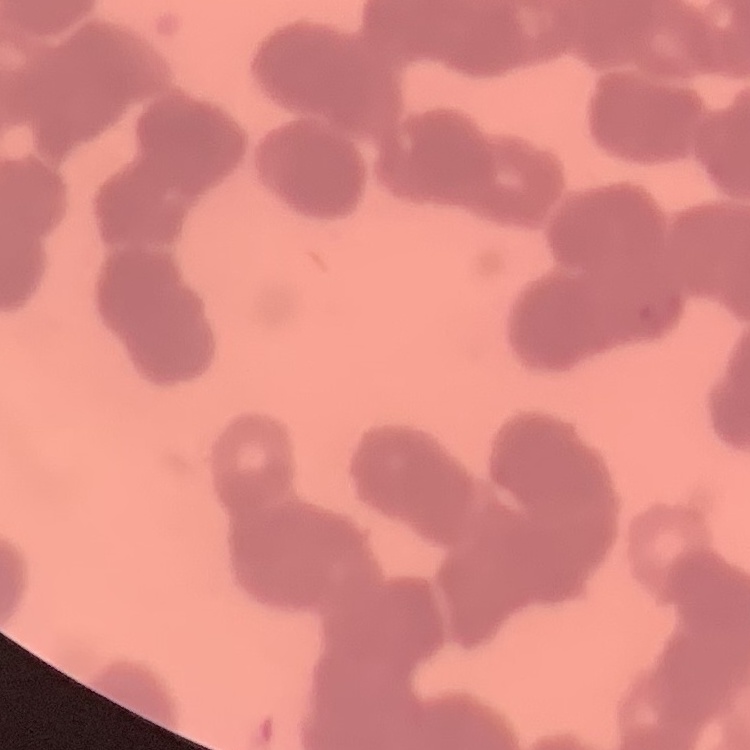

Summary:
  - Red blood cell morphology: rouleaux formation
  - Preparation: thin peripheral smear
  - Image type: square crop of a larger photomicrograph
  - Stain: Field's or Giemsa